Identify the blood parasite species.
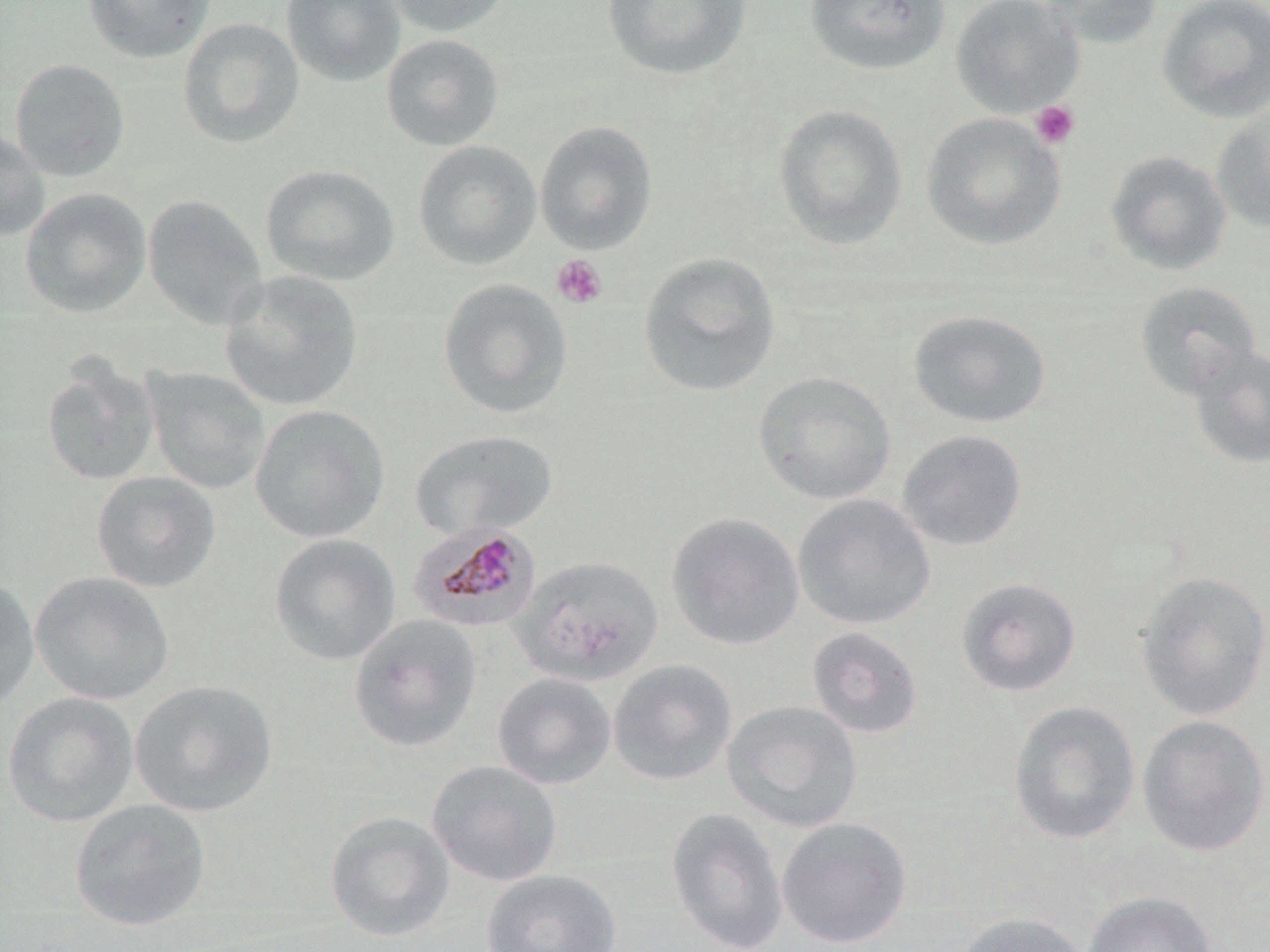

Plasmodium malariae.

Approximate bounding boxes as named x1/y1/x2/y2 corners in pixels. Plasmodium malariae-infected red blood cell locations: (x1=407, y1=522, x2=544, y2=635). Uninfected red blood cell locations: (x1=80, y1=0, x2=216, y2=64), (x1=281, y1=0, x2=405, y2=87), (x1=384, y1=0, x2=513, y2=37), (x1=601, y1=0, x2=752, y2=82), (x1=802, y1=0, x2=952, y2=77), (x1=949, y1=0, x2=1085, y2=119), (x1=1035, y1=0, x2=1163, y2=49), (x1=1156, y1=0, x2=1270, y2=123), (x1=177, y1=17, x2=305, y2=149), (x1=380, y1=33, x2=505, y2=152), (x1=9, y1=58, x2=130, y2=182), (x1=773, y1=104, x2=908, y2=251), (x1=1210, y1=106, x2=1270, y2=235), (x1=920, y1=112, x2=1066, y2=252), (x1=534, y1=120, x2=658, y2=255), (x1=0, y1=127, x2=51, y2=241), (x1=412, y1=140, x2=542, y2=271), (x1=1104, y1=149, x2=1233, y2=276), (x1=260, y1=164, x2=400, y2=287), (x1=19, y1=187, x2=152, y2=319), (x1=142, y1=193, x2=268, y2=329), (x1=637, y1=251, x2=782, y2=399), (x1=219, y1=270, x2=365, y2=412), (x1=436, y1=278, x2=574, y2=420), (x1=1132, y1=280, x2=1262, y2=400), (x1=907, y1=309, x2=1052, y2=429), (x1=1187, y1=343, x2=1270, y2=469), (x1=40, y1=357, x2=162, y2=487), (x1=142, y1=366, x2=271, y2=495), (x1=752, y1=371, x2=897, y2=505), (x1=249, y1=403, x2=391, y2=543), (x1=409, y1=429, x2=559, y2=541), (x1=896, y1=429, x2=1027, y2=552), (x1=90, y1=471, x2=222, y2=594), (x1=792, y1=494, x2=936, y2=630), (x1=666, y1=512, x2=805, y2=650), (x1=268, y1=533, x2=402, y2=666), (x1=513, y1=554, x2=664, y2=686), (x1=29, y1=571, x2=175, y2=706), (x1=1135, y1=571, x2=1270, y2=721), (x1=0, y1=573, x2=41, y2=712), (x1=956, y1=576, x2=1082, y2=697), (x1=348, y1=614, x2=483, y2=753), (x1=806, y1=626, x2=923, y2=738), (x1=607, y1=658, x2=737, y2=786), (x1=492, y1=671, x2=617, y2=790), (x1=129, y1=679, x2=278, y2=818), (x1=2, y1=691, x2=139, y2=827), (x1=721, y1=700, x2=863, y2=833), (x1=1008, y1=700, x2=1141, y2=845), (x1=1137, y1=714, x2=1270, y2=858), (x1=426, y1=760, x2=564, y2=887), (x1=69, y1=798, x2=211, y2=932), (x1=665, y1=807, x2=789, y2=951), (x1=325, y1=810, x2=455, y2=942), (x1=777, y1=816, x2=913, y2=949), (x1=481, y1=868, x2=622, y2=952), (x1=1081, y1=890, x2=1219, y2=952), (x1=950, y1=911, x2=1091, y2=952). Platelet locations: (x1=1030, y1=100, x2=1080, y2=150), (x1=551, y1=254, x2=608, y2=309). Single field of view. Thin blood smear. Optical microscopy. Image is 1270×952 pixels. May-Grünwald-Giemsa stain. 1000x magnification.